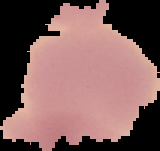

{
  "image_size": "160×151 pixels",
  "malaria_status": "uninfected",
  "image_type": "cell region segmented out of the field of view; surrounding area masked to black",
  "preparation": "thin blood smear"
}